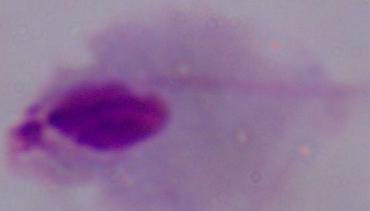

A trichomonad is seen. 1000x magnification. Micrograph.